Locate every Plasmodium parasite.
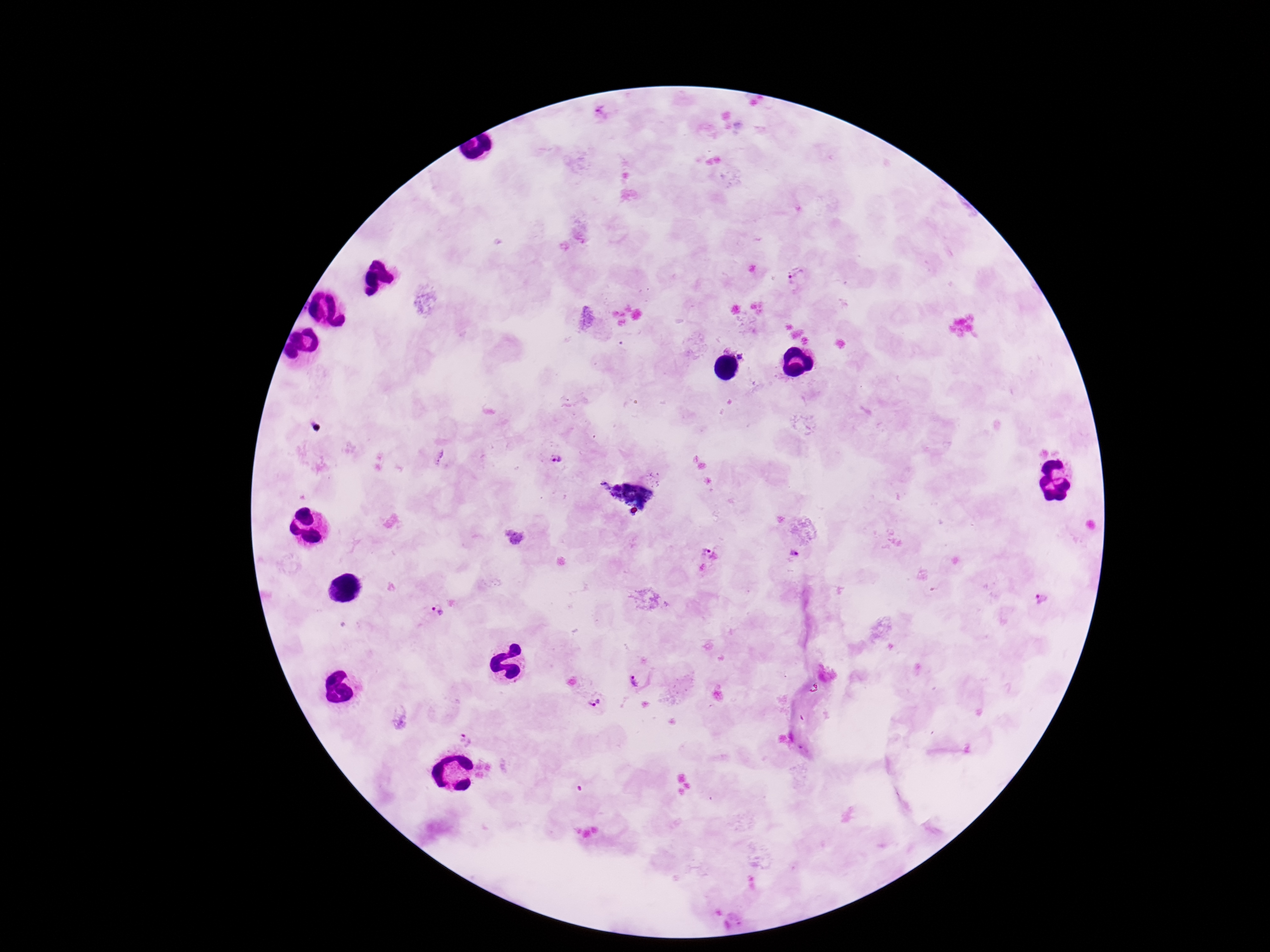

Approximate centers as (x, y) in pixels.
Plasmodium parasites: (603, 118), (798, 275), (744, 354), (553, 459), (794, 553), (709, 554), (1044, 598), (438, 611), (636, 679), (597, 700), (465, 740).

Giemsa-stained preparation. Single field of view. Thick peripheral-blood smear. Patient malaria status: infected. Image is 1270×952 pixels. Smartphone photograph taken through the microscope eyepiece. 100x magnification.